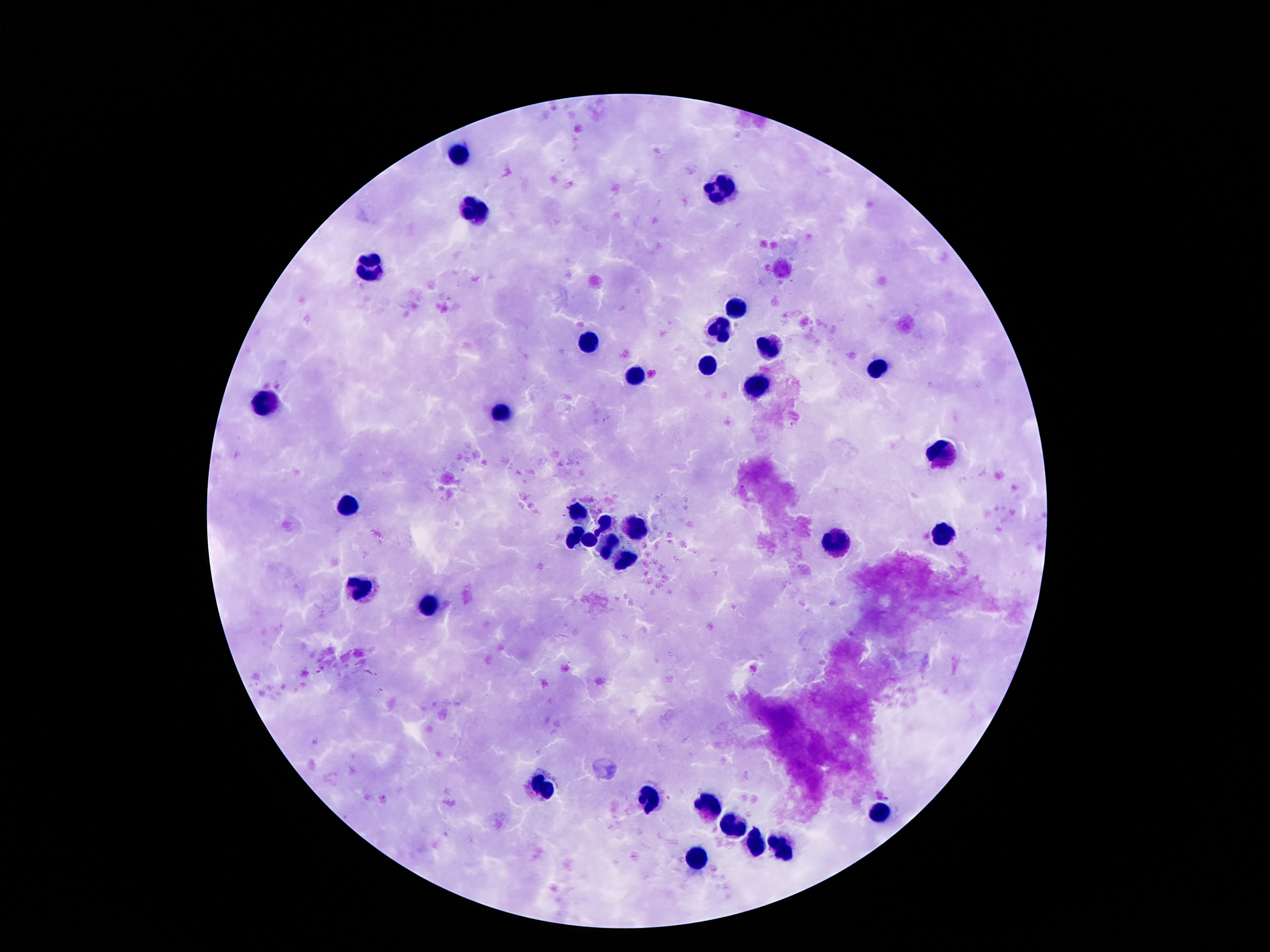
Approximate centers as (x, y) in pixels. Leukocyte locations: (458, 153), (716, 189), (470, 211), (365, 264), (735, 308), (720, 330), (588, 338), (767, 344), (706, 367), (878, 369), (636, 375), (754, 388), (265, 403), (500, 417), (941, 453), (347, 506), (573, 514), (603, 521), (636, 524), (573, 537), (943, 537), (590, 541), (836, 544), (609, 548), (626, 560), (363, 590), (431, 602), (540, 786), (651, 799), (710, 808), (878, 812), (731, 826), (754, 840), (781, 849), (695, 861). Photographed through the microscope eyepiece with a smartphone camera. Thick blood film. Patient malaria status: uninfected. One field from this slide. Image is 1270×952 pixels. Giemsa-stained preparation. 100x magnification.